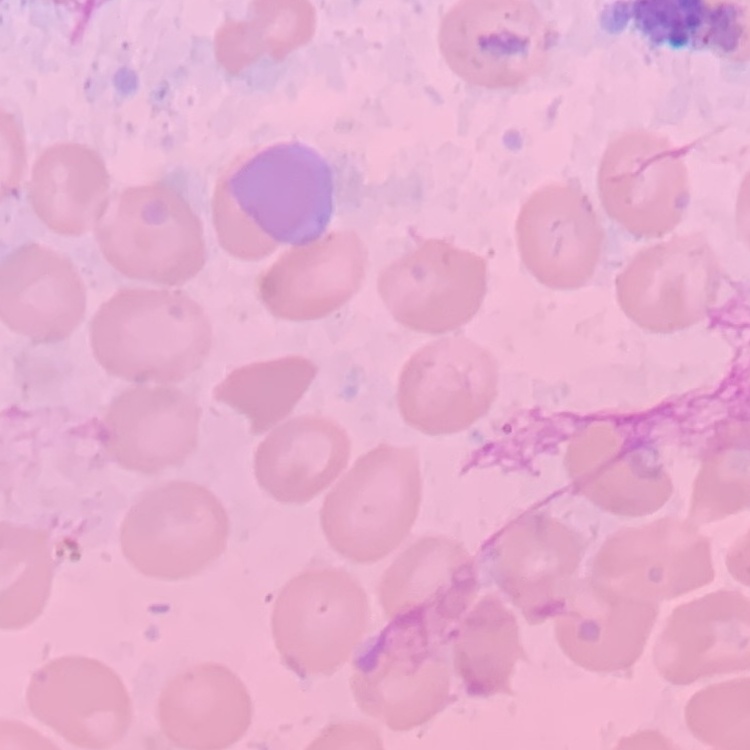
Summary:
  - Erythrocyte morphology: no rouleaux formation
  - Image type: square crop of a larger photomicrograph
  - Stain: Field's or Giemsa
  - Preparation: thin blood film